Outline each blood parasite and name the species.
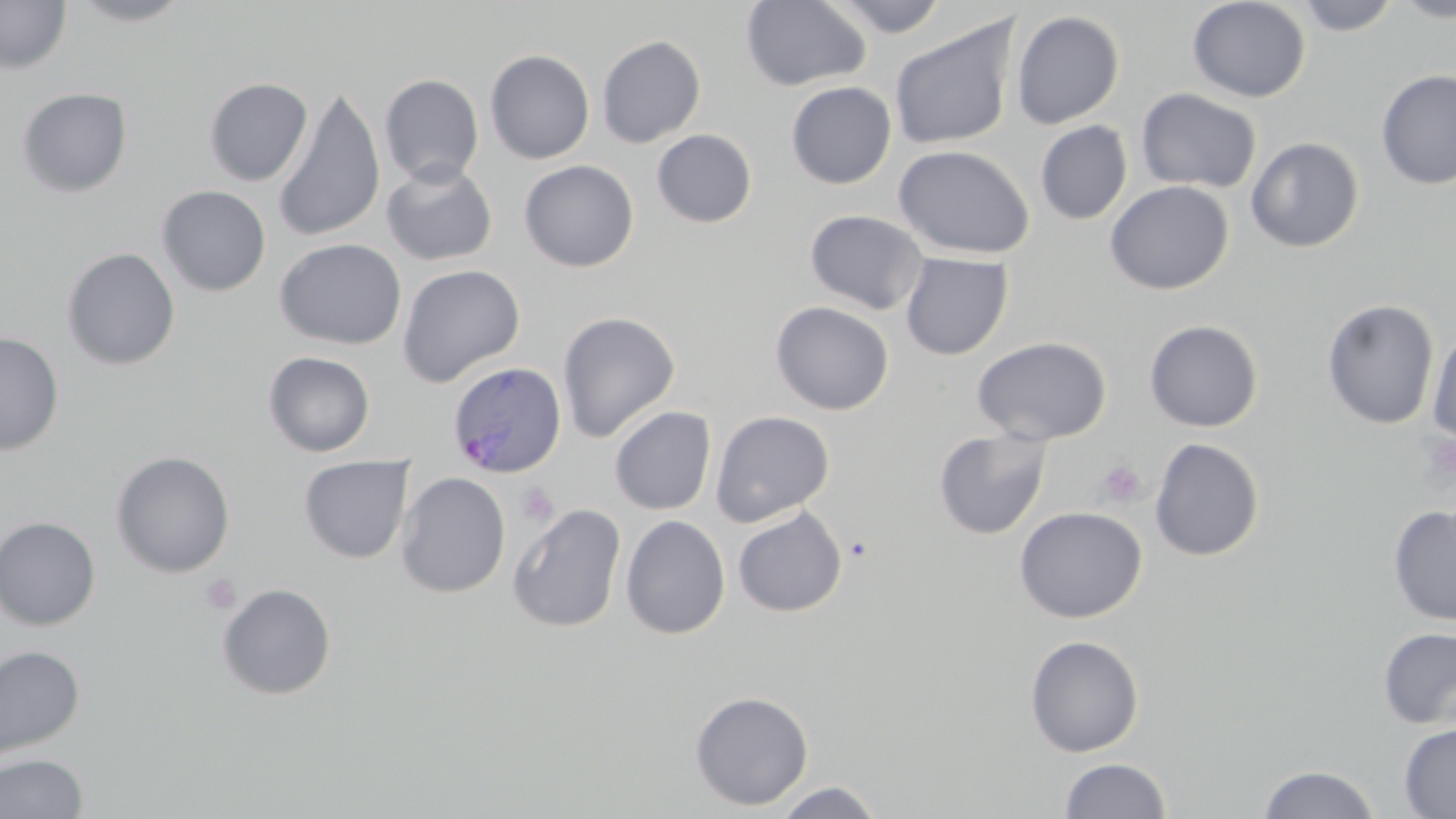

Approximate bounding boxes as (x1,y1)-(x2,y2) corner pairs in pixels.
Plasmodium ovale-infected red blood cells: (447,361)-(568,479).
No Plasmodium falciparum, Plasmodium malariae, Plasmodium vivax, Babesia divergens, or Trypanosoma brucei observed.

slide-level diagnosis = Plasmodium ovale
uninfected red blood cell locations = approximate bounding boxes as (x1,y1)-(x2,y2) corner pairs in pixels: (66,0)-(198,26), (741,0)-(871,91), (828,0)-(949,37), (1187,0)-(1311,103), (1293,0)-(1402,35), (1389,0)-(1456,22), (0,1)-(72,75), (1011,10)-(1124,129), (888,15)-(1020,151), (596,35)-(706,148), (485,49)-(595,163), (1376,69)-(1456,190), (379,74)-(484,187), (204,77)-(313,186), (786,81)-(897,188), (272,86)-(386,242), (17,87)-(133,197), (1137,88)-(1262,193), (1035,121)-(1132,224), (651,129)-(757,228), (1246,137)-(1365,253), (893,145)-(1035,259), (519,160)-(639,271), (381,161)-(498,266), (1105,180)-(1233,294), (157,185)-(271,296), (805,209)-(929,314), (274,238)-(407,350), (62,247)-(180,371), (900,252)-(1013,360), (396,264)-(526,387), (1322,299)-(1439,430), (770,301)-(895,415), (557,311)-(680,442), (1144,319)-(1264,432), (1426,324)-(1456,447), (0,332)-(64,455), (972,335)-(1111,445), (263,352)-(375,456), (610,406)-(716,515), (710,410)-(835,527), (933,428)-(1052,540), (1149,437)-(1265,562), (111,450)-(235,578), (298,455)-(414,563), (395,471)-(511,598), (507,503)-(627,633), (1387,505)-(1456,626), (732,506)-(847,617), (1014,506)-(1147,623), (620,515)-(731,639), (0,516)-(101,630), (216,583)-(337,700), (1377,628)-(1456,730), (1024,635)-(1144,757), (0,644)-(86,764), (689,690)-(814,810), (1399,723)-(1456,817), (0,753)-(89,818), (1058,758)-(1172,818), (1256,764)-(1381,819), (772,781)-(885,819)
field of view = one of a larger specimen
preparation = thin blood smear
modality = optical microscopy
platelet locations = approximate bounding boxes as (x1,y1)-(x2,y2) corner pairs in pixels: (1420,433)-(1456,483), (1097,459)-(1146,508), (516,482)-(560,526), (201,574)-(240,614)
magnification = 1000x
image size = 1456×819 pixels
stain = May-Grünwald-Giemsa